Assess this cell for malaria.
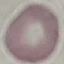

Uninfected.

Automatically extracted cell patch, resized to 64 × 64 pixels. Photographed with a smartphone camera at the microscope eyepiece. Thin smear of blood. Giemsa-stained preparation.